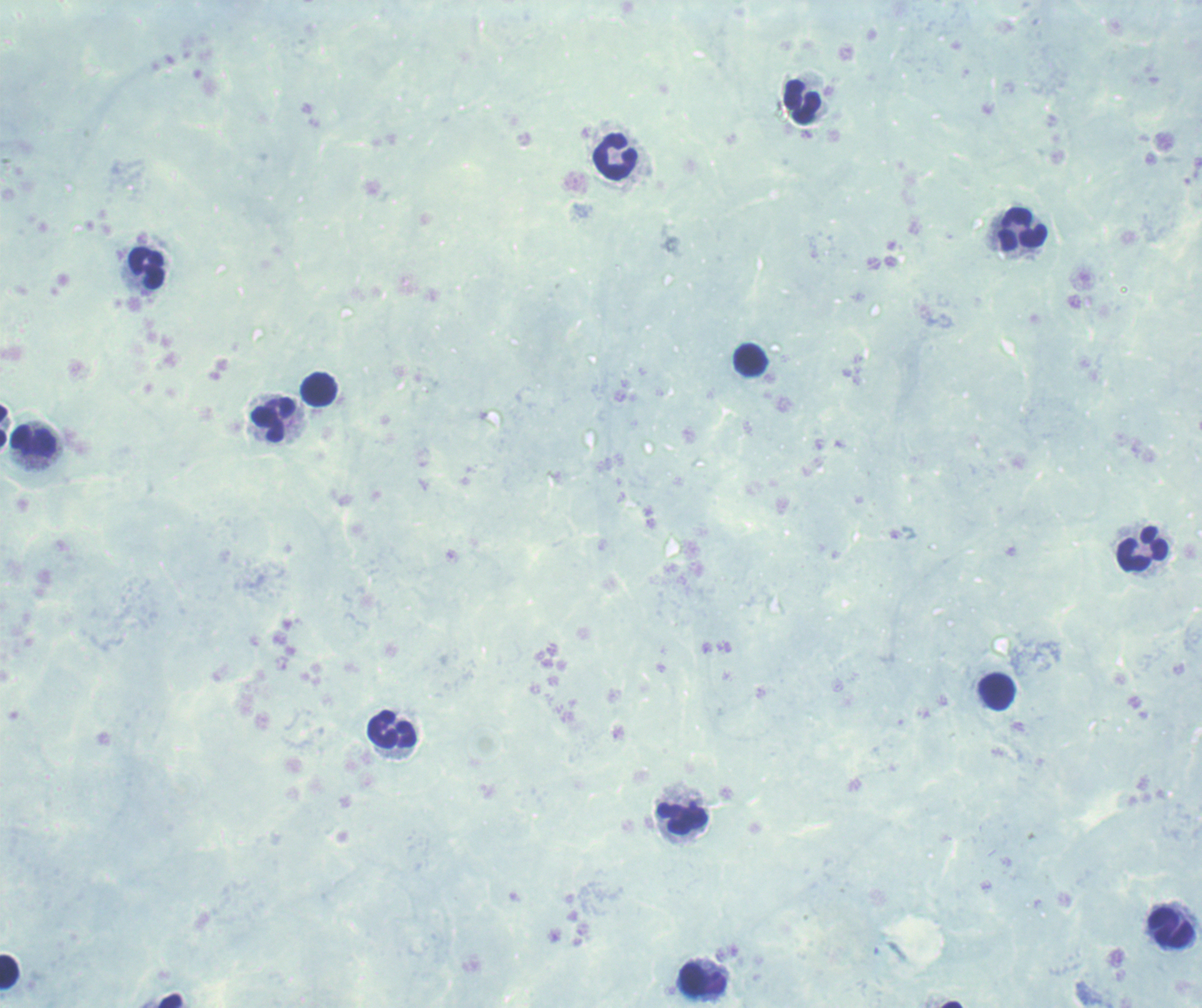

coordinate format = approximate centers as (x, y) in pixels
leukocyte locations = (802, 102), (615, 157), (1023, 229), (146, 268), (750, 360), (318, 389), (273, 420), (3, 425), (33, 440), (1143, 549), (997, 691), (392, 729), (682, 818), (1170, 929), (9, 971), (703, 979)
magnification = 100x
context = previously used in an actual diagnosis
result = no malaria parasites seen
background quality = poor
field of view = one from this slide
stain = Romanowsky
preparation = thick blood smear
image size = 1202×1008 pixels